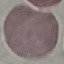
Malaria status: uninfected. Thin blood smear. Photographed with a smartphone camera at the microscope eyepiece. Cell patch, automatically extracted from a larger field of view and resized to 64 × 64 pixels. Giemsa-stained preparation.